State the blood parasite species.
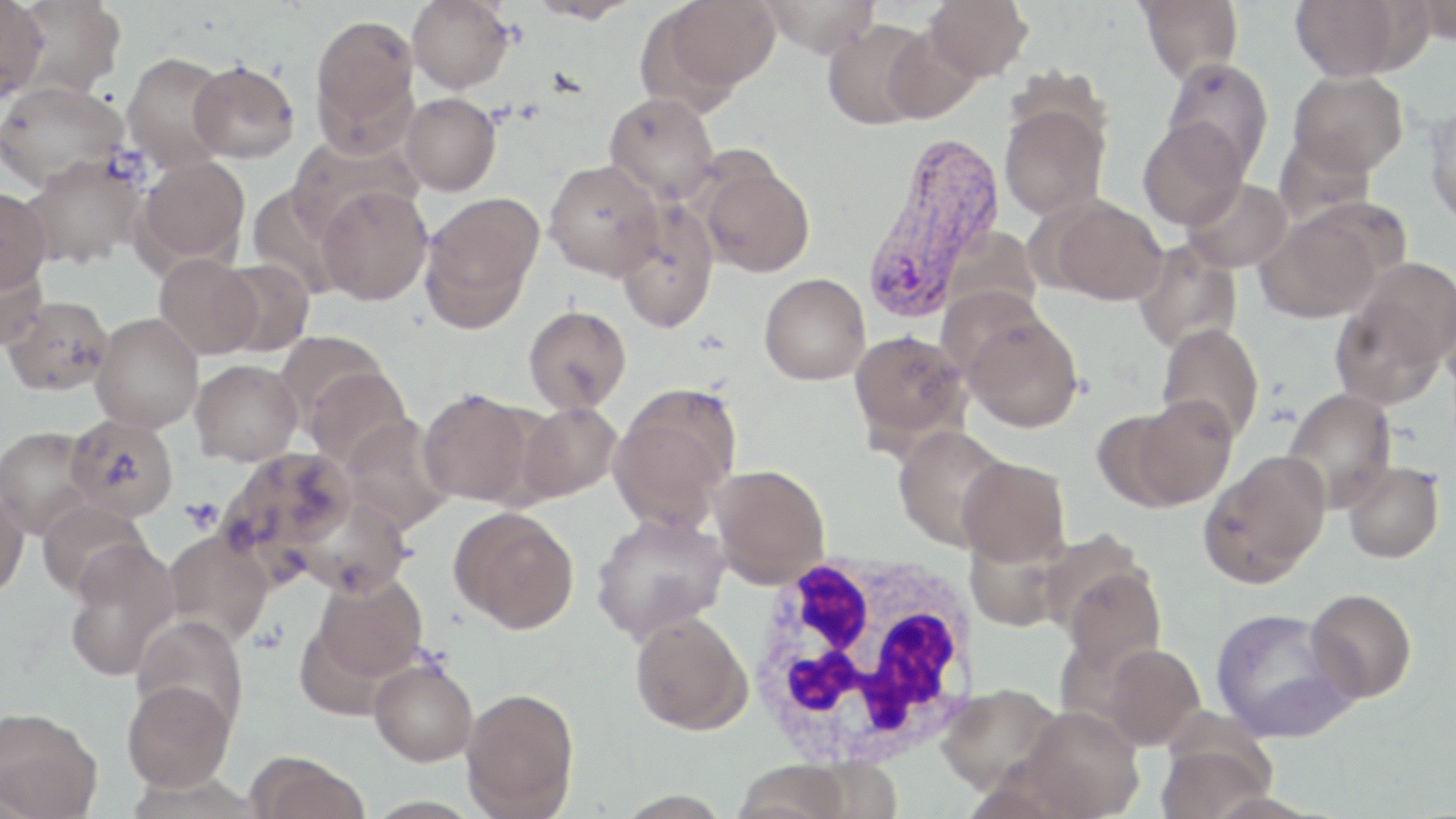

Plasmodium vivax.

modality = light microscopy
magnification = 1000x
image size = 1456×819 pixels
Plasmodium vivax-infected red blood cell locations = approximate bounding boxes as (x1, y1, x2, y2) in pixels: (860, 129, 1008, 324)
platelet locations = approximate bounding boxes as (x1, y1, x2, y2) in pixels: (180, 499, 223, 532)
preparation = thin blood smear
stain = May-Grünwald-Giemsa
field of view = one of a larger specimen
uninfected red blood cell locations = approximate bounding boxes as (x1, y1, x2, y2) in pixels: (8, 0, 127, 99), (407, 0, 515, 93), (525, 0, 638, 24), (652, 0, 781, 98), (758, 0, 881, 57), (924, 0, 1032, 81), (1135, 0, 1243, 84), (1289, 0, 1419, 80), (1411, 0, 1456, 46), (0, 1, 48, 102), (309, 13, 421, 150), (821, 18, 933, 130), (882, 26, 982, 124), (121, 53, 233, 173), (1160, 56, 1274, 175), (189, 61, 299, 163), (1288, 70, 1409, 176), (0, 81, 128, 191), (399, 92, 501, 196), (604, 92, 720, 203), (999, 103, 1110, 221), (1423, 103, 1456, 229), (1137, 117, 1249, 230), (286, 135, 421, 238), (137, 154, 250, 268), (22, 155, 147, 269), (543, 159, 665, 281), (697, 160, 815, 277), (1182, 177, 1293, 273), (246, 184, 353, 299), (316, 186, 433, 306), (0, 187, 51, 292), (418, 192, 544, 332), (1045, 196, 1168, 305), (614, 200, 720, 335), (1257, 201, 1396, 324), (941, 226, 1042, 327), (1132, 239, 1243, 355), (0, 254, 48, 350), (154, 254, 261, 359), (213, 258, 315, 357), (759, 272, 871, 385), (1331, 284, 1449, 409), (936, 286, 1053, 381), (4, 295, 114, 396), (523, 305, 632, 413), (961, 311, 1083, 432), (90, 312, 203, 433), (1156, 323, 1265, 443), (848, 330, 972, 450), (276, 331, 389, 428), (190, 359, 303, 466), (303, 366, 413, 471), (609, 386, 741, 530), (418, 388, 542, 507), (1281, 388, 1398, 513), (1117, 396, 1238, 510), (516, 401, 623, 503), (66, 413, 179, 520), (339, 414, 454, 533), (0, 425, 98, 539), (893, 426, 1011, 552), (220, 446, 358, 570), (1198, 450, 1331, 588), (956, 457, 1070, 566), (1342, 461, 1445, 564), (709, 464, 830, 588), (0, 483, 29, 600), (290, 491, 412, 598), (37, 498, 152, 600), (448, 505, 579, 634), (590, 511, 731, 645), (163, 529, 274, 644), (63, 545, 179, 683), (1059, 559, 1166, 676), (309, 572, 428, 688), (1305, 588, 1417, 703), (1209, 607, 1357, 742), (629, 610, 753, 735), (131, 615, 248, 733), (1102, 643, 1205, 749), (368, 657, 479, 767), (122, 678, 235, 792), (937, 683, 1063, 795), (460, 687, 580, 819), (1018, 706, 1145, 817), (0, 707, 103, 819), (1156, 733, 1277, 819), (245, 751, 369, 819), (733, 759, 853, 819)
white blood cell locations = approximate bounding boxes as (x1, y1, x2, y2) in pixels: (742, 546, 986, 772)